Locate every malaria parasite.
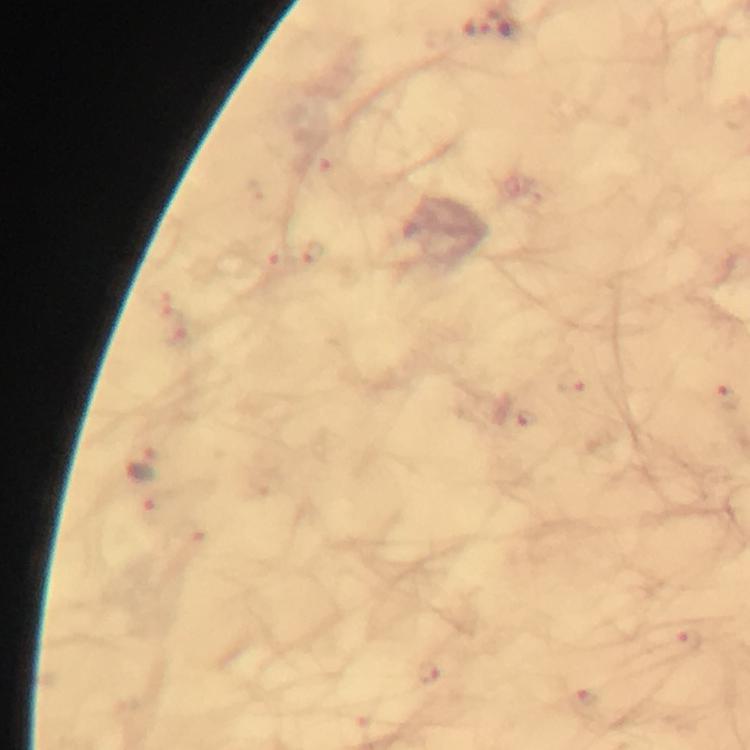

Approximate centers as (x, y) in pixels.
Malaria parasites: (477, 28), (336, 173), (315, 253), (275, 264), (574, 382), (728, 400), (526, 417), (145, 464), (147, 513), (192, 539), (691, 642), (430, 674), (587, 704).

Summary:
  - Context: from a malaria diagnostic workup
  - Cropped from: one field of view
  - Preparation: thick smear
  - Immersion oil: applied
  - Stain: Giemsa
  - Magnification: 100x
  - Image size: 750×750 pixels
  - Capture: smartphone mounted on the microscope